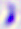
modality = micrograph
identification = Toxoplasma gondii
magnification = 400x